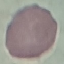

Summary:
  - Malaria status: uninfected
  - Image type: cell patch, automatically extracted from a larger field of view and resized to 64 × 64 pixels
  - Preparation: thin blood film
  - Capture: smartphone camera at the microscope eyepiece
  - Stain: Giemsa